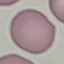 Malaria status: uninfected. Acquired by smartphone through the microscope eyepiece. Giemsa stain. Thin smear of blood. Automatically extracted cell patch, resized to 64 × 64 pixels.